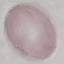

Summary:
  - Result: no malaria parasites seen
  - Image type: automatically extracted cell patch, resized to 64 × 64 pixels
  - Capture: smartphone camera at the microscope eyepiece
  - Preparation: thin blood smear
  - Stain: Giemsa